State which parasite is depicted.
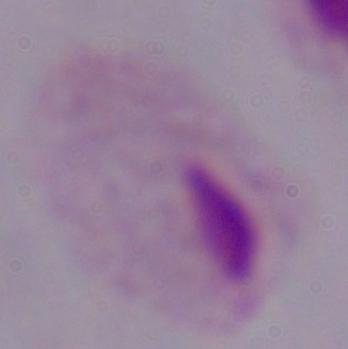

This is a trichomonad.

1000x magnification. Micrograph.